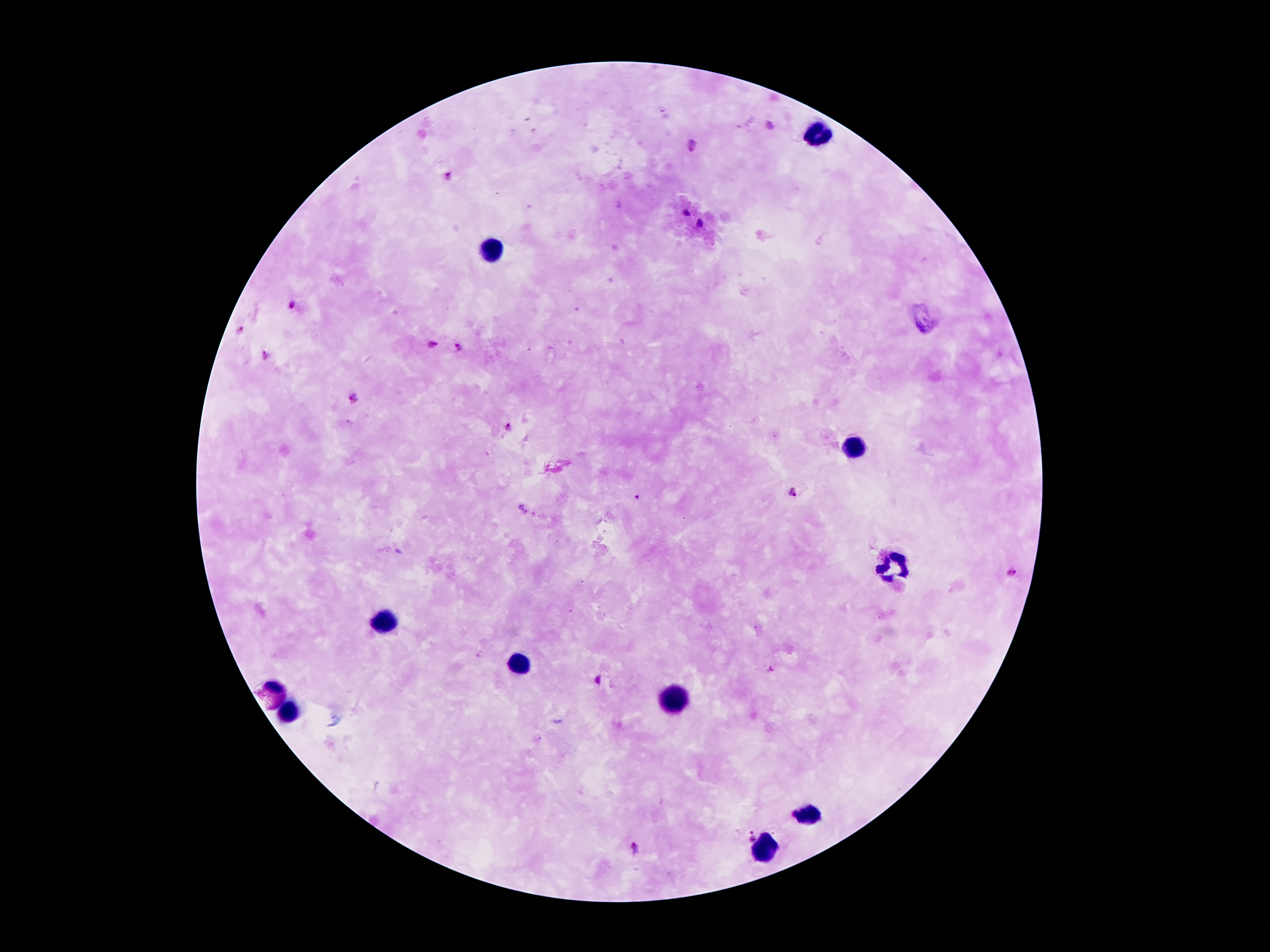
Approximate object centers, in pixels from the top-left corner. Malaria parasite locations: (x=770, y=126), (x=689, y=145), (x=448, y=174), (x=686, y=213), (x=700, y=225), (x=291, y=305), (x=240, y=331), (x=434, y=343), (x=458, y=347), (x=265, y=354), (x=353, y=397), (x=508, y=427), (x=793, y=492), (x=637, y=496), (x=1012, y=573), (x=771, y=669), (x=598, y=680), (x=749, y=835), (x=635, y=849). Leukocyte locations: (x=817, y=135), (x=488, y=245), (x=852, y=447), (x=893, y=564), (x=387, y=623), (x=522, y=662), (x=277, y=686), (x=677, y=700), (x=291, y=714), (x=805, y=812), (x=761, y=847). 100x magnification. Photographed through the microscope eyepiece with a smartphone camera. Single field of view. Patient malaria status: positive for Plasmodium falciparum. Thick blood smear. Giemsa stain. Image is 1270×952 pixels.